Identify the parasite.
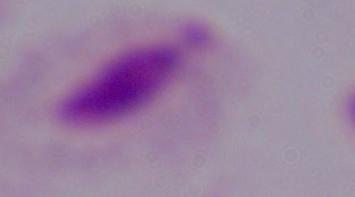

A trichomonad.

Summary:
  - Modality: micrograph
  - Magnification: 1000x